Classify this cell by malaria status.
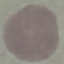

Uninfected.

Thin smear of blood. Photographed with a smartphone camera at the microscope eyepiece. Giemsa-stained preparation. Cell patch, automatically extracted from a larger field of view and resized to 64 × 64 pixels.